Point out every Plasmodium parasite and every leukocyte.
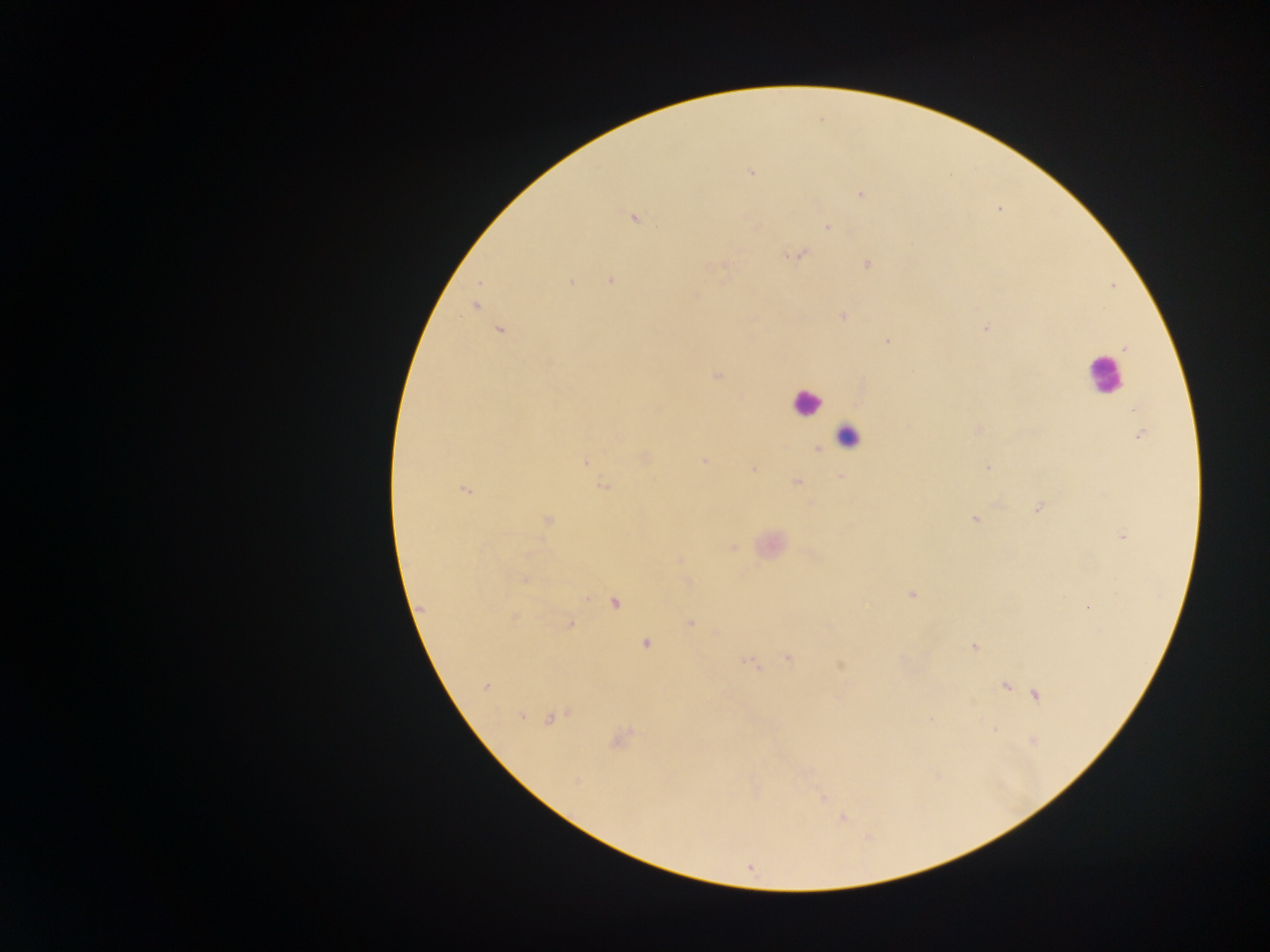

Approximate centers as x y in pixels.
Plasmodium parasites: 750 171; 861 194; 632 217; 827 226; 798 254; 867 263; 725 266; 610 280; 571 281; 695 296; 475 306; 844 315; 986 328; 499 330; 887 342; 1125 347; 717 375; 978 429; 1140 434; 817 449; 646 459; 584 461; 703 461; 988 467; 753 469; 840 476; 796 481; 602 484; 464 490; 811 503; 1037 508; 974 518; 546 520; 1122 535; 733 548; 678 560; 524 580; 911 594; 615 603; 1088 606; 420 609; 513 615; 690 623; 569 624; 646 643; 973 646; 788 658; 745 661; 839 664; 754 665; 486 685; 1005 686; 1036 694; 521 715; 552 716; 619 738; 1032 740; 574 781; 822 798; 842 818; 749 866.
Leukocytes: 1105 374; 805 402; 848 436.

preparation: thick blood smear
field_of_view: single
country: Ghana
image_size: 1270×952 pixels
capture: mobile-phone photograph through a microscope